Name the blood parasite species.
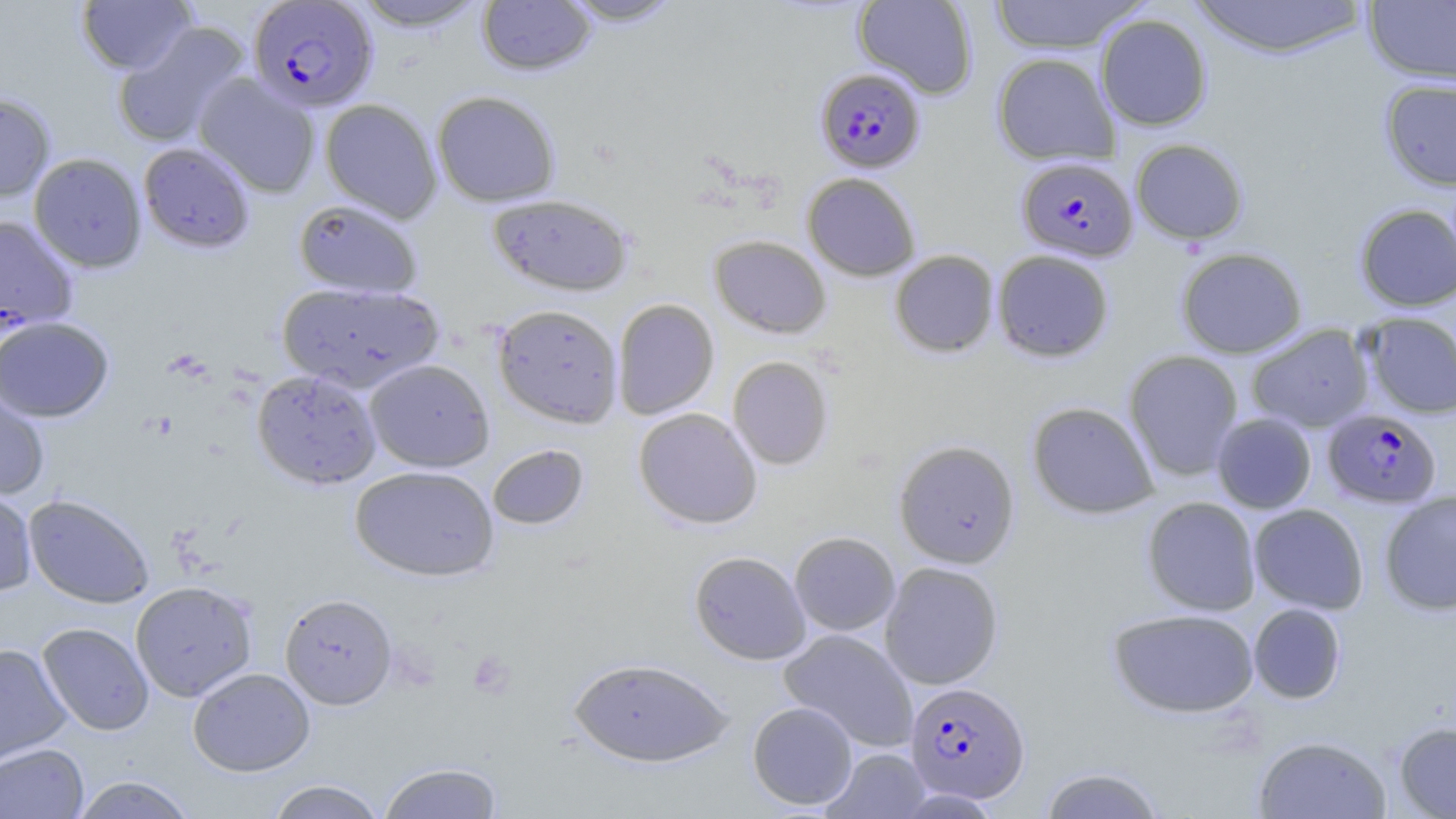

Plasmodium falciparum.

Summary:
  - Coordinate format: approximate bounding boxes as [x1, y1, x2, y2] in pixels
  - Uninfected red blood cell locations: [350, 0, 491, 32], [477, 0, 596, 76], [557, 0, 685, 26], [853, 0, 978, 99], [988, 0, 1148, 54], [1186, 0, 1372, 60], [77, 1, 196, 75], [1363, 1, 1456, 85], [1096, 13, 1212, 131], [112, 20, 250, 149], [991, 52, 1120, 166], [193, 74, 321, 198], [1380, 78, 1456, 191], [431, 90, 561, 207], [0, 93, 56, 201], [319, 98, 442, 223], [1130, 139, 1249, 245], [138, 142, 255, 253], [28, 153, 147, 273], [802, 172, 921, 281], [487, 193, 634, 297], [294, 199, 422, 298], [1355, 204, 1456, 311], [0, 214, 79, 331], [709, 235, 832, 338], [1176, 247, 1307, 358], [993, 249, 1114, 362], [890, 250, 999, 358], [278, 281, 444, 392], [612, 298, 720, 420], [492, 304, 623, 429], [1361, 312, 1456, 418], [0, 317, 114, 422], [1247, 324, 1374, 432], [1124, 350, 1243, 481], [727, 356, 833, 471], [365, 359, 495, 472], [252, 369, 381, 489], [0, 381, 52, 501], [1027, 401, 1159, 520], [633, 408, 763, 529], [1211, 413, 1316, 514], [893, 439, 1020, 568], [487, 443, 589, 531], [350, 465, 499, 581], [0, 488, 38, 598], [1379, 491, 1456, 615], [23, 493, 155, 609], [1143, 497, 1262, 616], [1248, 504, 1368, 614], [789, 531, 900, 635], [689, 550, 811, 665], [880, 562, 1004, 690], [130, 580, 258, 702], [279, 593, 397, 709], [1248, 603, 1346, 704], [1108, 608, 1259, 718], [37, 622, 154, 736], [778, 629, 918, 751], [0, 642, 72, 766], [567, 656, 735, 767], [188, 667, 315, 776], [747, 701, 858, 810], [1393, 721, 1456, 818], [1253, 735, 1392, 819], [0, 743, 89, 819], [822, 747, 931, 818], [377, 761, 504, 819], [1038, 766, 1167, 819], [69, 775, 199, 818], [265, 780, 387, 819]
  - Plasmodium falciparum-infected red blood cell locations: [247, 1, 379, 113], [815, 68, 926, 173], [1016, 156, 1138, 262], [1322, 409, 1442, 509], [904, 681, 1030, 804]
  - Platelet locations: [467, 651, 515, 698]
  - Image size: 1456×819 pixels
  - Modality: optical microscopy
  - Magnification: 1000x
  - Preparation: thin blood smear
  - Stain: May-Grünwald-Giemsa
  - Field of view: single